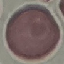

Malaria status: uninfected. Photographed with a smartphone camera at the microscope eyepiece. Thin blood smear. Giemsa-stained preparation. Automatically extracted cell patch, resized to 64 × 64 pixels.